Comment on the morphology of the red blood cells.
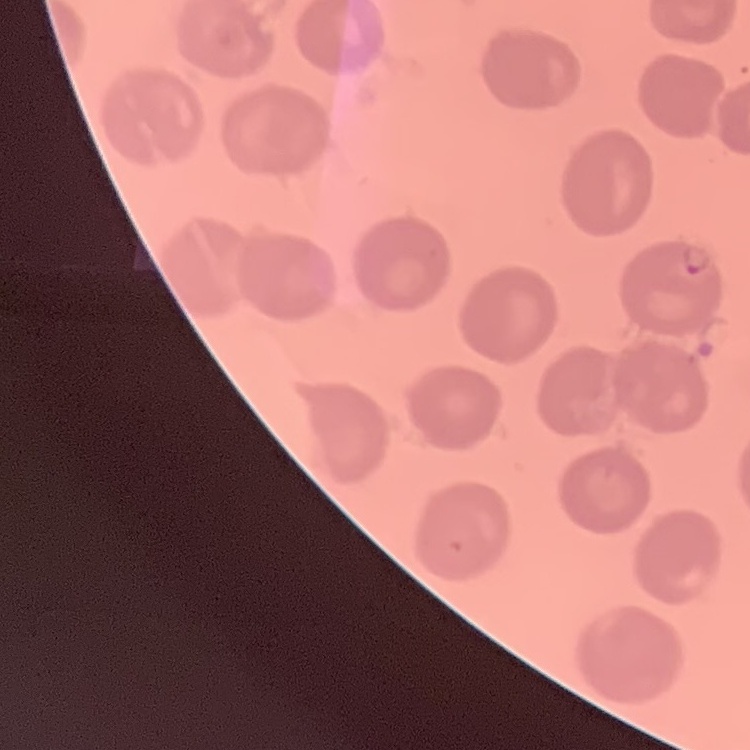

They show no rouleaux formation.

Summary:
  - Image type: one tile cut from a larger photomicrograph
  - Preparation: thin blood film
  - Stain: Field's or Giemsa